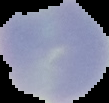 Malaria status: uninfected. Segmented cell region on a black background. From a thin blood film. Image is 109×103 pixels.